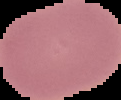
Summary:
  - Result: no Plasmodium parasites detected
  - Image size: 121×100 pixels
  - Image type: cell region segmented out of the field of view; surrounding area masked to black
  - Preparation: thin blood film